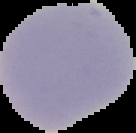

Summary:
  - Malaria status: uninfected
  - Image size: 136×133 pixels
  - Image type: segmented cell region on a black background
  - Preparation: thin blood smear